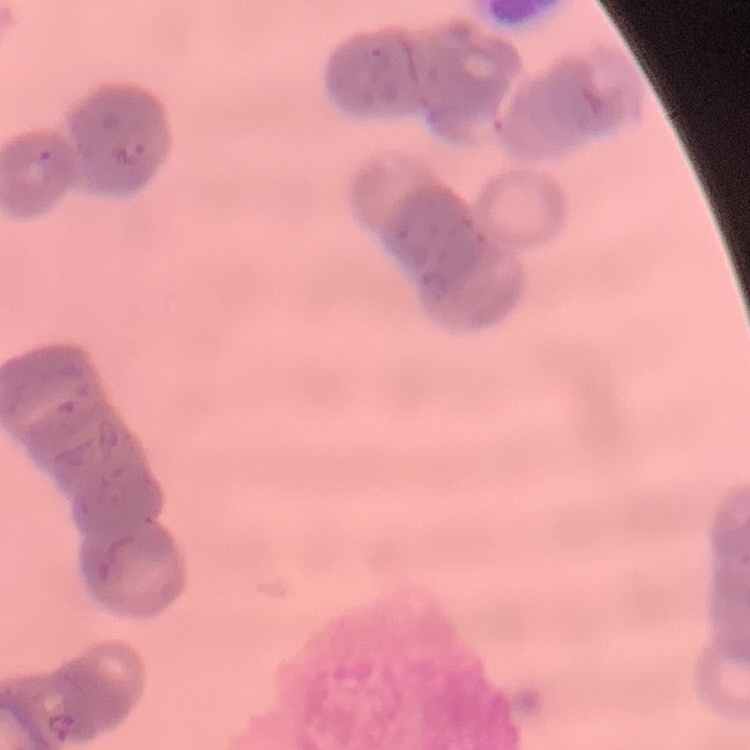

The red blood cells exhibit rouleaux formation. Field's or Giemsa stain. Thin blood film. Square crop of a larger photomicrograph.